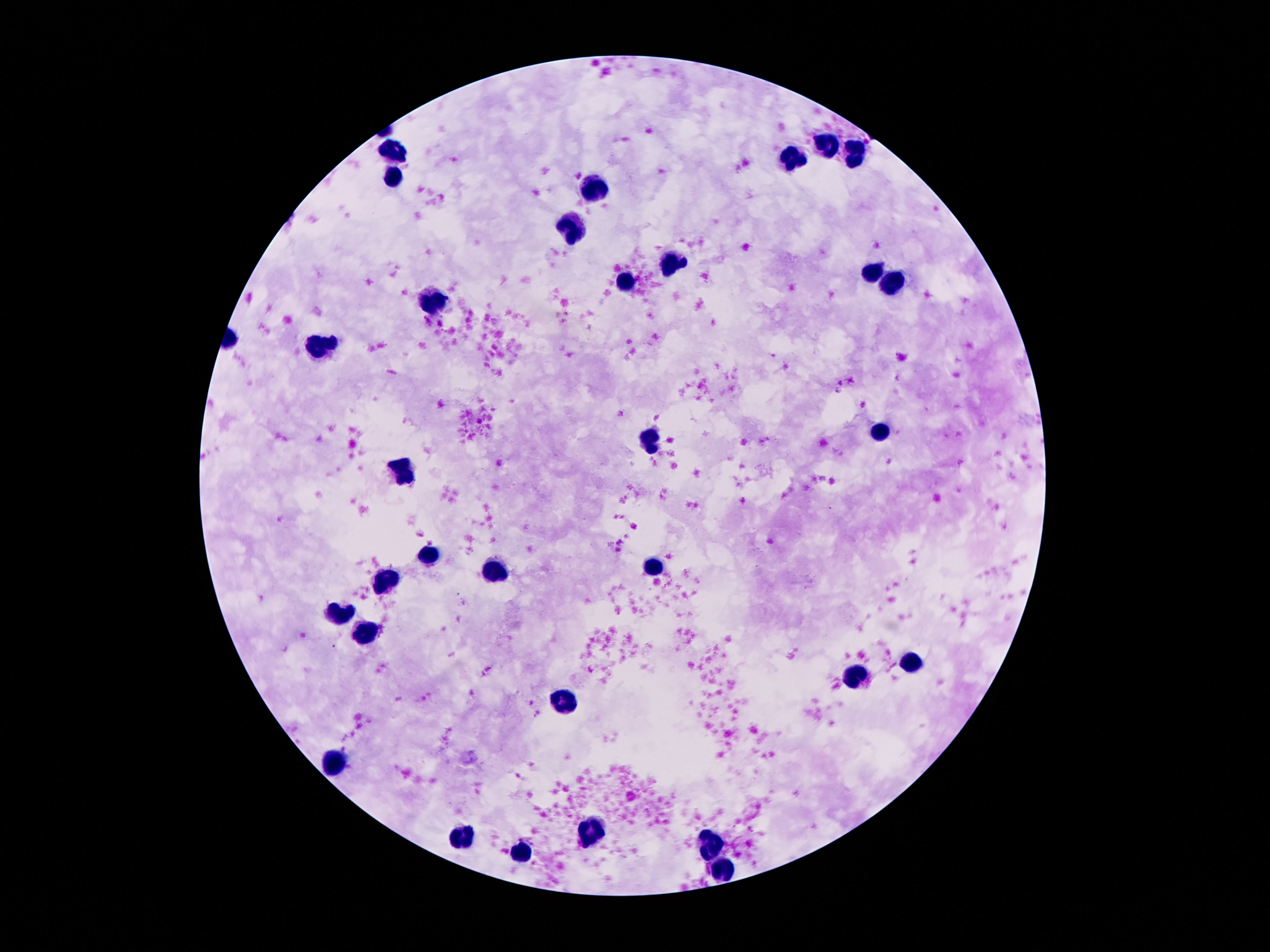

Approximate centers as (x, y) in pixels.
Summary:
  - Leukocyte locations: (827, 143), (395, 150), (857, 155), (791, 159), (392, 180), (591, 193), (575, 230), (672, 262), (873, 275), (892, 281), (630, 284), (432, 302), (325, 346), (880, 431), (649, 440), (406, 468), (432, 555), (652, 566), (495, 574), (385, 583), (339, 616), (365, 633), (910, 661), (859, 678), (565, 702), (332, 761), (588, 829), (462, 835), (714, 839), (521, 853), (722, 868)
  - Magnification: 100x
  - Patient malaria status: not infected
  - Image size: 1270×952 pixels
  - Capture: smartphone camera through the microscope eyepiece
  - Preparation: thick blood film
  - Stain: Giemsa
  - Field of view: single